Identify the parasite.
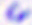

This is Toxoplasma gondii.

400x magnification. Micrograph.